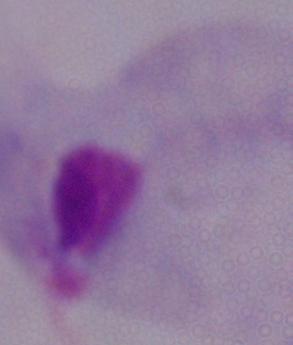
{
  "identification": "trichomonad",
  "modality": "micrograph",
  "magnification": "1000x"
}